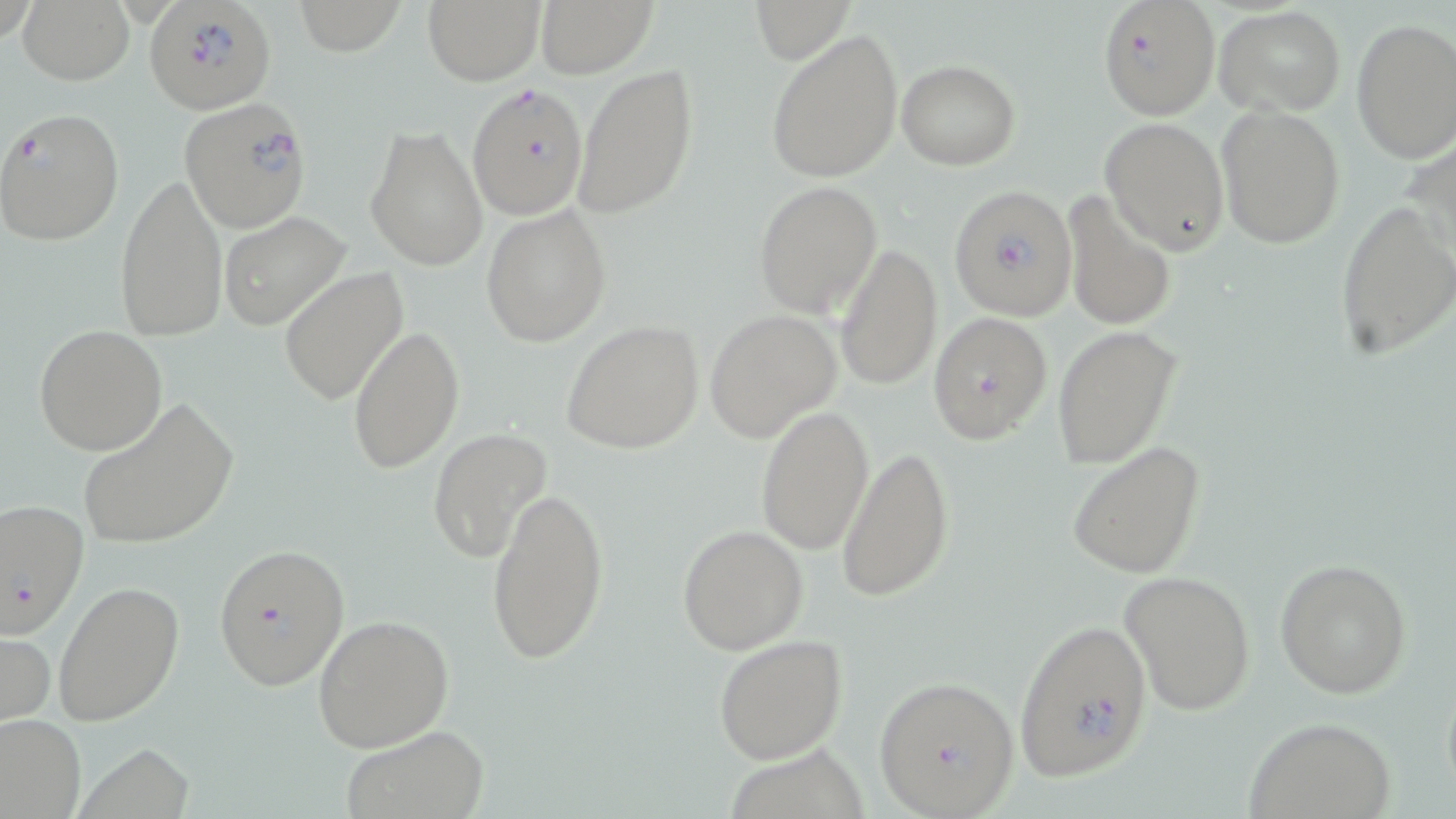 Approximate bounding boxes as named x1/y1/x2/y2 corners in pixels. Plasmodium falciparum-infected red blood cell locations: (x1=144, y1=0, x2=276, y2=115), (x1=1098, y1=0, x2=1222, y2=119), (x1=466, y1=81, x2=588, y2=222), (x1=179, y1=100, x2=312, y2=241), (x1=0, y1=107, x2=125, y2=248), (x1=949, y1=185, x2=1078, y2=321), (x1=927, y1=311, x2=1054, y2=445), (x1=1, y1=498, x2=89, y2=638), (x1=212, y1=542, x2=350, y2=692), (x1=1013, y1=620, x2=1154, y2=778), (x1=873, y1=673, x2=1020, y2=818). Uninfected red blood cell locations: (x1=17, y1=0, x2=135, y2=85), (x1=294, y1=0, x2=406, y2=55), (x1=423, y1=0, x2=544, y2=86), (x1=534, y1=0, x2=657, y2=78), (x1=752, y1=0, x2=855, y2=63), (x1=1217, y1=5, x2=1346, y2=114), (x1=1352, y1=16, x2=1456, y2=162), (x1=765, y1=28, x2=904, y2=184), (x1=896, y1=59, x2=1021, y2=169), (x1=570, y1=64, x2=698, y2=222), (x1=1217, y1=104, x2=1346, y2=250), (x1=1100, y1=116, x2=1230, y2=254), (x1=365, y1=124, x2=490, y2=271), (x1=115, y1=172, x2=227, y2=343), (x1=753, y1=180, x2=883, y2=317), (x1=1063, y1=189, x2=1177, y2=333), (x1=1335, y1=200, x2=1455, y2=359), (x1=482, y1=205, x2=610, y2=347), (x1=217, y1=212, x2=351, y2=329), (x1=834, y1=242, x2=942, y2=391), (x1=279, y1=268, x2=409, y2=404), (x1=704, y1=310, x2=843, y2=443), (x1=560, y1=319, x2=704, y2=454), (x1=34, y1=323, x2=167, y2=455), (x1=349, y1=324, x2=463, y2=474), (x1=1051, y1=324, x2=1181, y2=468), (x1=77, y1=399, x2=238, y2=551), (x1=755, y1=404, x2=873, y2=555), (x1=428, y1=427, x2=553, y2=563), (x1=1066, y1=439, x2=1207, y2=580), (x1=837, y1=446, x2=955, y2=602), (x1=485, y1=483, x2=610, y2=666), (x1=677, y1=523, x2=808, y2=654), (x1=1274, y1=557, x2=1412, y2=698), (x1=1119, y1=569, x2=1256, y2=717), (x1=52, y1=580, x2=185, y2=728), (x1=311, y1=613, x2=455, y2=752), (x1=0, y1=627, x2=56, y2=732), (x1=712, y1=634, x2=849, y2=763), (x1=0, y1=713, x2=84, y2=818), (x1=1243, y1=716, x2=1397, y2=819), (x1=340, y1=725, x2=491, y2=819). Slide-level diagnosis: Plasmodium falciparum. Image is 1456×819 pixels. Single field of view. Optical microscopy. 1000x magnification. May-Grünwald-Giemsa stain. Thin blood film.